Assess the morphology of the erythrocytes.
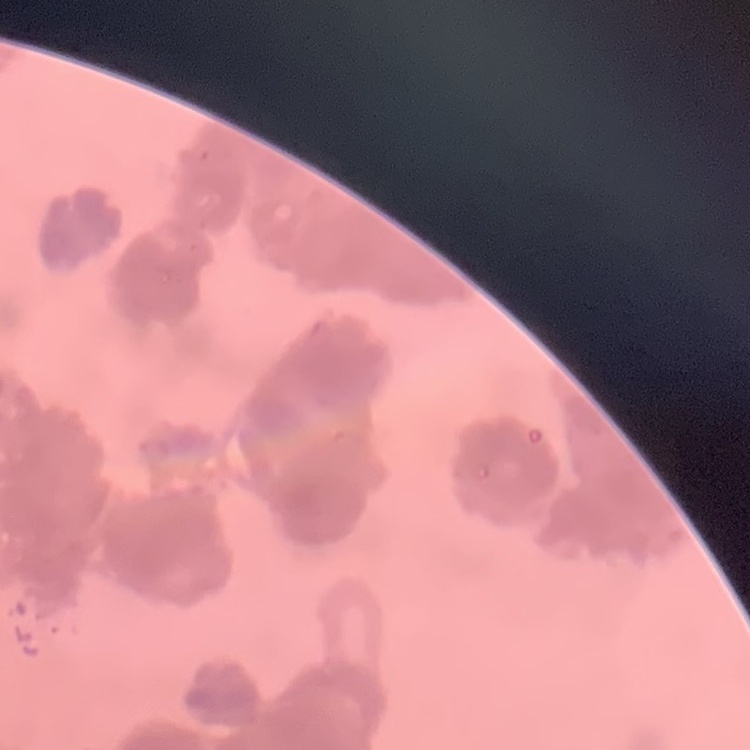

Rouleaux formation.

Square crop of a larger photomicrograph. Stained with either Field's or Giemsa. Thin peripheral smear.